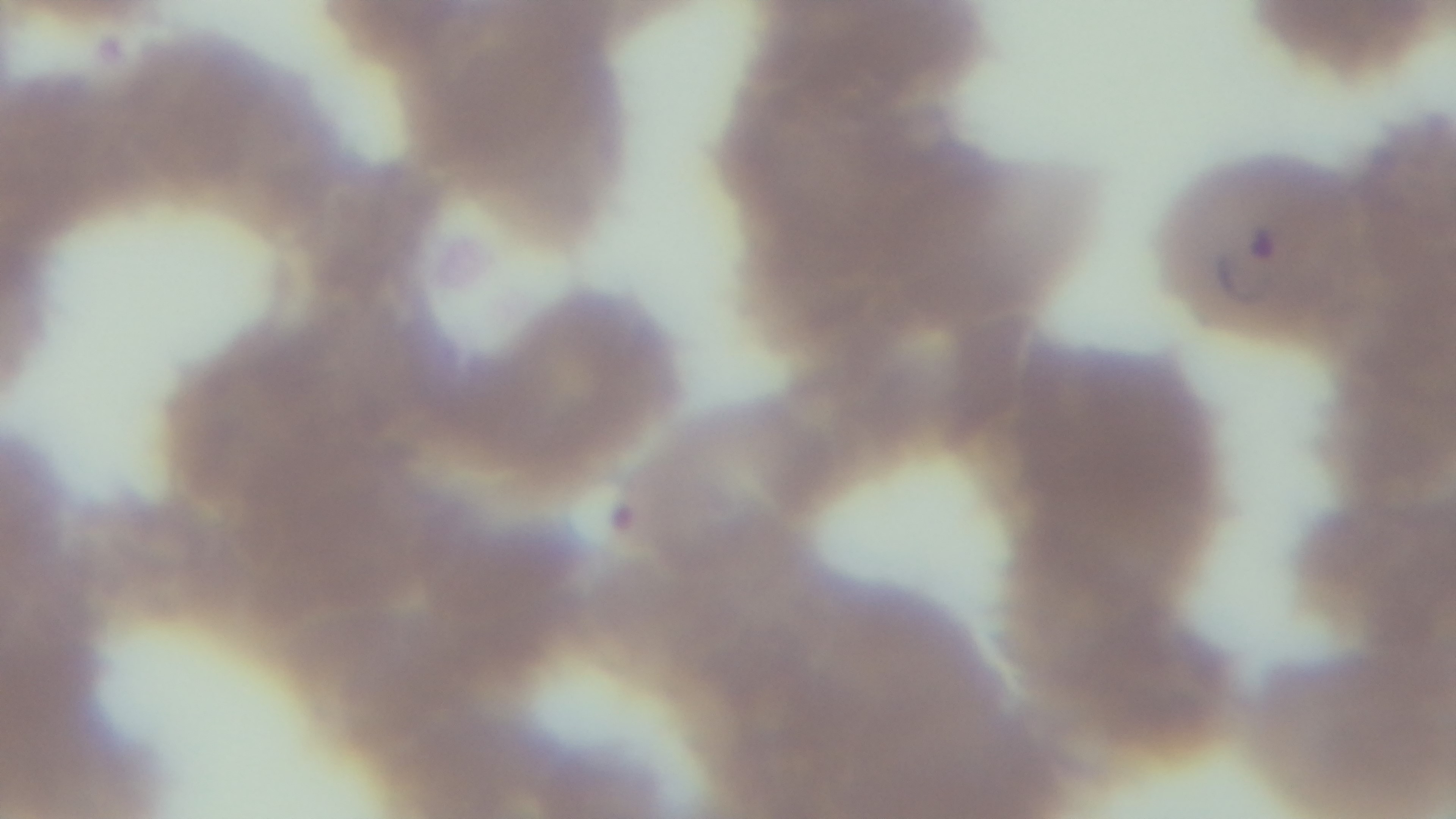

preparation = thin smear
modality = light microscopy
malaria status = infected
field of view = one from the slide
capture = mounted 4K digital camera
objective = 100x oil immersion
stain = Giemsa